State which parasite is depicted.
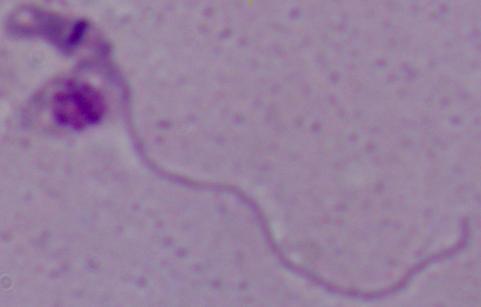

Leishmania.

Micrograph. 1000x magnification.